Comment on the morphology of the red blood cells.
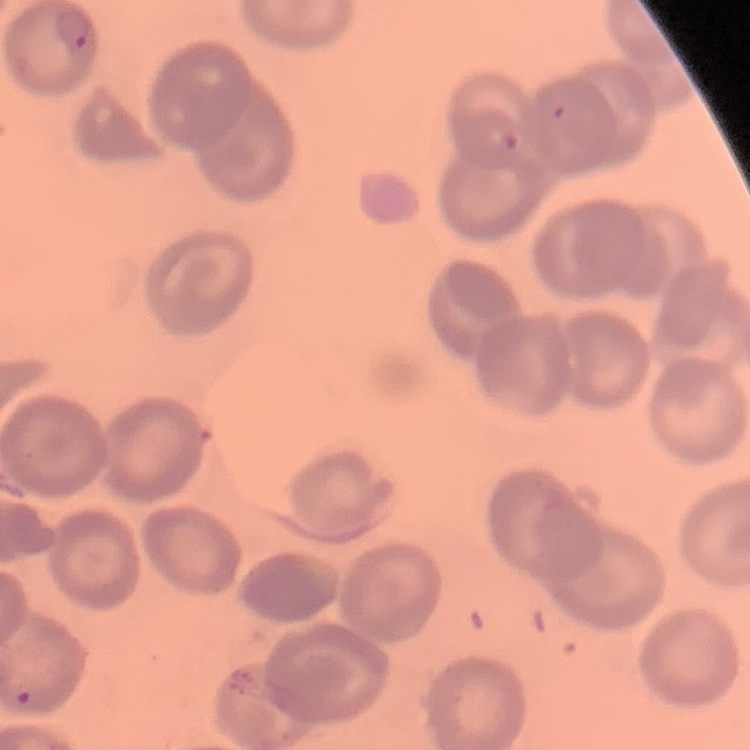

They show no rouleaux formation.

Stained with either Field's or Giemsa. One tile cut from a larger photomicrograph. Thin blood film.